Identify the parasite.
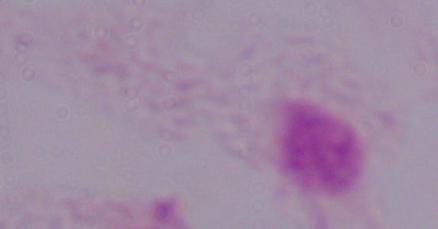
This is a trichomonad.

{
  "magnification": "1000x",
  "modality": "photomicrograph"
}